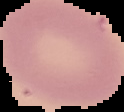

Summary:
  - Preparation: thin blood film
  - Image type: segmented cell region on a black background
  - Image size: 124×112 pixels
  - Result: no Plasmodium parasites detected